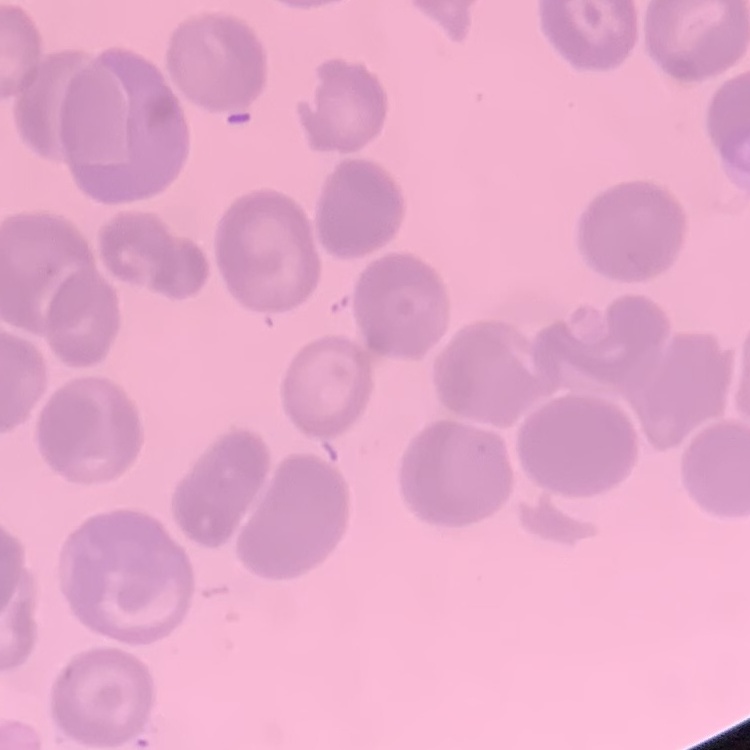

Summary:
  - Red blood cell morphology: no rouleaux formation
  - Preparation: thin peripheral smear
  - Stain: Field's or Giemsa
  - Image type: square crop of a larger photomicrograph